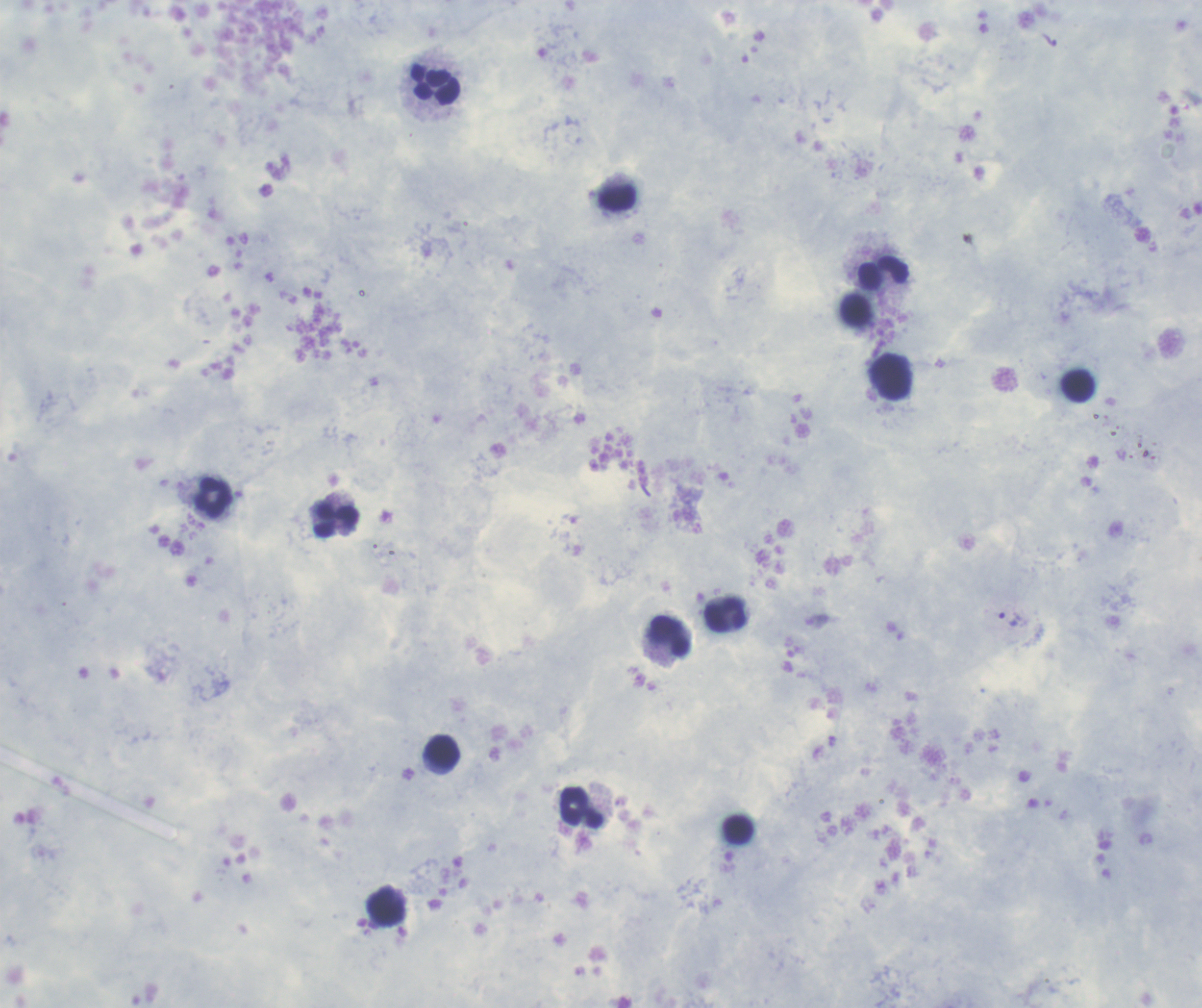
Approximate centers as (x, y) in pixels. Leukocyte locations: (435, 85), (618, 197), (883, 273), (891, 377), (1079, 386), (214, 498), (336, 519), (726, 614), (669, 637), (442, 750), (581, 807), (387, 907). Trophozoite locations: (1009, 619). Romanowsky-stained preparation. Result: positive for Plasmodium parasites. Background quality: good. Thick smear of blood. Image is 1202×1008 pixels. Coloration quality: good. One field from this slide. Captured at 100x magnification. Previously used in an actual diagnosis.